Assess this cell for malaria.
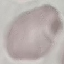
It is uninfected.

Thin blood film. Automatically extracted cell patch, resized to 64 × 64 pixels. Photographed with a smartphone camera at the microscope eyepiece. Giemsa-stained preparation.